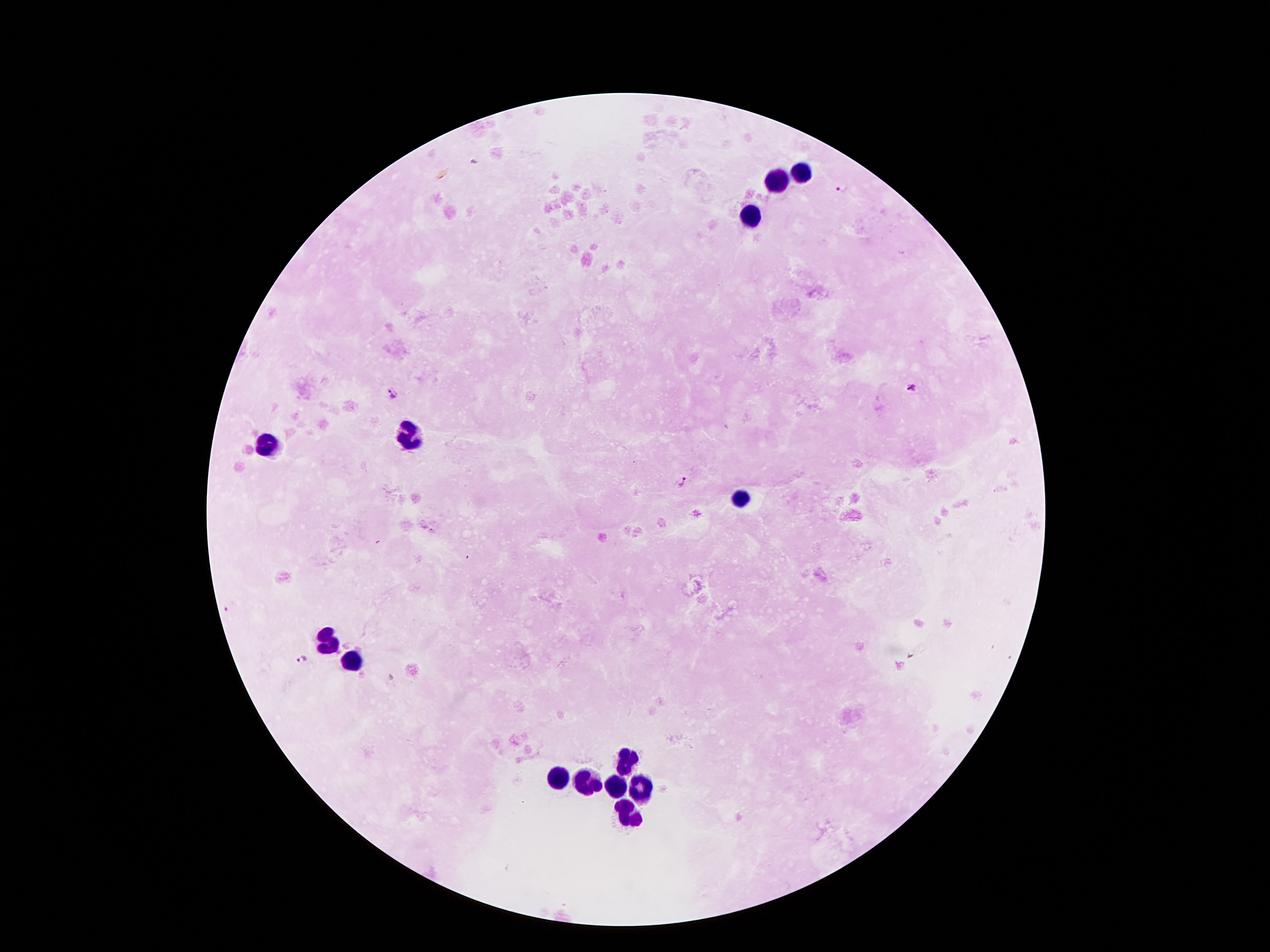 Approximate centers as {x, y} in pixels. Malaria parasite locations: {841, 188}, {912, 389}, {392, 393}, {682, 481}, {230, 606}, {300, 660}. Leukocyte locations: {803, 173}, {778, 180}, {753, 216}, {408, 434}, {268, 444}, {742, 502}, {327, 640}, {358, 661}, {628, 761}, {556, 777}, {583, 784}, {617, 784}, {642, 789}, {629, 813}. Image is 1270×952 pixels. Patient malaria status: positive for Plasmodium falciparum. Photographed through the microscope eyepiece with a smartphone camera. Single field of view. Giemsa stain. Thick blood film. 100x magnification.